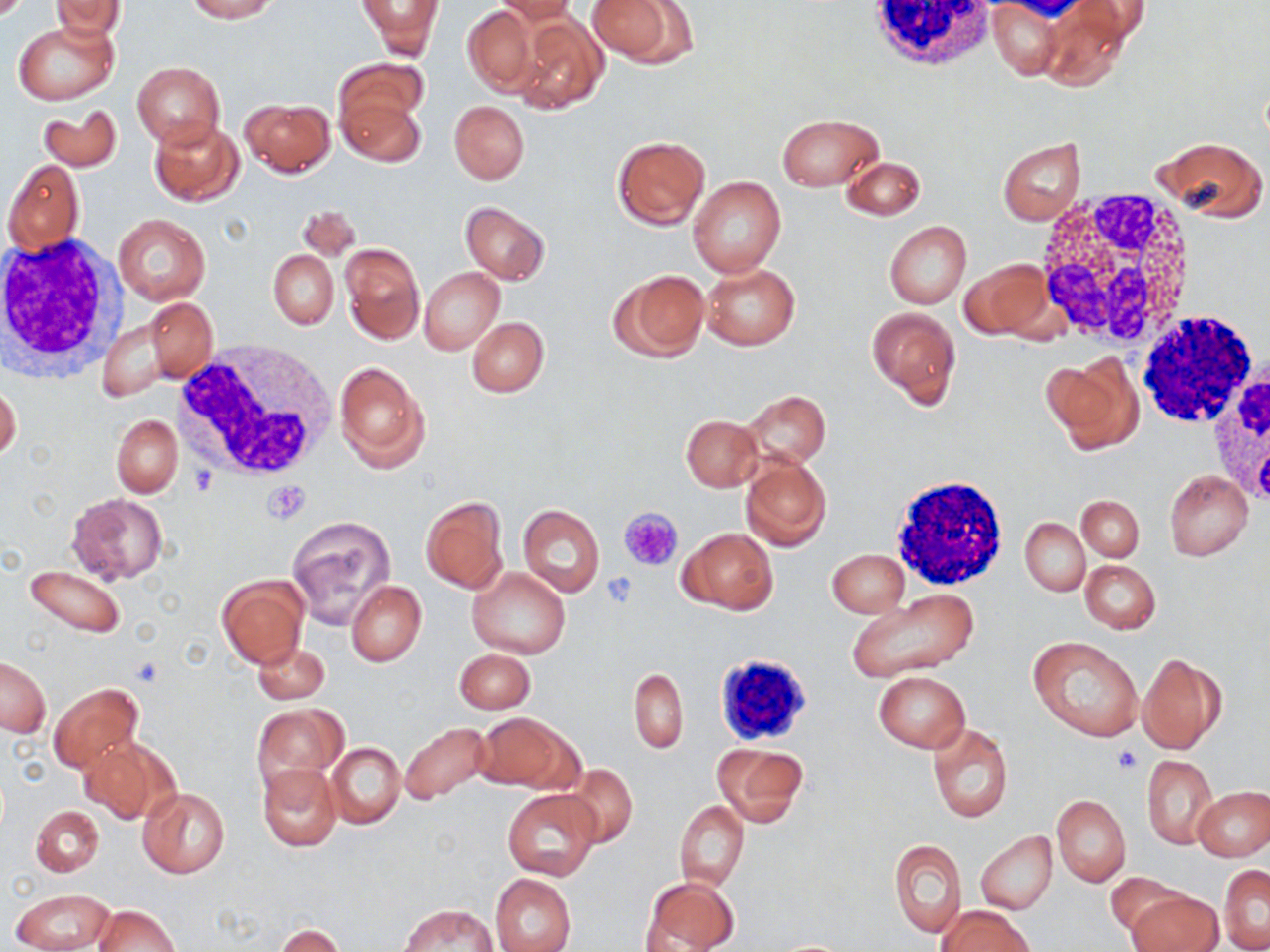

Summary:
  - Coordinate format: approximate bounding boxes as named x1/y1/x2/y2 corners in pixels
  - Platelet locations: (x1=265, y1=481, x2=309, y2=523), (x1=619, y1=506, x2=684, y2=571), (x1=600, y1=571, x2=640, y2=607), (x1=1113, y1=744, x2=1143, y2=773)
  - Uninfected red blood cell locations: (x1=185, y1=0, x2=278, y2=22), (x1=358, y1=0, x2=444, y2=58), (x1=494, y1=0, x2=576, y2=23), (x1=585, y1=0, x2=696, y2=67), (x1=988, y1=0, x2=1065, y2=79), (x1=51, y1=1, x2=126, y2=41), (x1=1039, y1=3, x2=1140, y2=89), (x1=463, y1=5, x2=538, y2=94), (x1=512, y1=11, x2=608, y2=115), (x1=13, y1=20, x2=118, y2=105), (x1=337, y1=57, x2=428, y2=135), (x1=133, y1=62, x2=224, y2=150), (x1=338, y1=96, x2=426, y2=167), (x1=240, y1=97, x2=334, y2=177), (x1=449, y1=100, x2=530, y2=183), (x1=37, y1=106, x2=122, y2=172), (x1=777, y1=113, x2=882, y2=191), (x1=149, y1=118, x2=245, y2=207), (x1=612, y1=136, x2=709, y2=229), (x1=1154, y1=136, x2=1267, y2=223), (x1=998, y1=138, x2=1086, y2=226), (x1=841, y1=155, x2=926, y2=221), (x1=3, y1=159, x2=85, y2=257), (x1=688, y1=175, x2=787, y2=278), (x1=298, y1=202, x2=361, y2=264), (x1=461, y1=202, x2=549, y2=285), (x1=440, y1=209, x2=536, y2=327), (x1=113, y1=212, x2=211, y2=306), (x1=884, y1=220, x2=971, y2=308), (x1=340, y1=242, x2=425, y2=344), (x1=268, y1=250, x2=339, y2=328), (x1=959, y1=258, x2=1057, y2=344), (x1=701, y1=264, x2=800, y2=350), (x1=421, y1=268, x2=504, y2=356), (x1=609, y1=270, x2=710, y2=360), (x1=142, y1=297, x2=219, y2=387), (x1=866, y1=306, x2=961, y2=405), (x1=467, y1=315, x2=548, y2=397), (x1=97, y1=317, x2=174, y2=402), (x1=1043, y1=358, x2=1142, y2=454), (x1=333, y1=359, x2=430, y2=473), (x1=0, y1=384, x2=21, y2=462), (x1=743, y1=390, x2=830, y2=469), (x1=111, y1=414, x2=182, y2=497), (x1=680, y1=414, x2=763, y2=492), (x1=707, y1=429, x2=824, y2=532), (x1=741, y1=454, x2=832, y2=552), (x1=1165, y1=469, x2=1252, y2=560), (x1=66, y1=492, x2=169, y2=585), (x1=1077, y1=495, x2=1144, y2=560), (x1=420, y1=496, x2=508, y2=593), (x1=518, y1=504, x2=605, y2=597), (x1=286, y1=515, x2=396, y2=627), (x1=1021, y1=518, x2=1089, y2=596), (x1=679, y1=528, x2=777, y2=614), (x1=827, y1=549, x2=909, y2=618), (x1=1080, y1=560, x2=1159, y2=633), (x1=23, y1=564, x2=125, y2=637), (x1=467, y1=567, x2=569, y2=658), (x1=216, y1=575, x2=308, y2=668), (x1=346, y1=581, x2=426, y2=666), (x1=845, y1=590, x2=980, y2=683), (x1=1029, y1=636, x2=1143, y2=742), (x1=253, y1=642, x2=330, y2=704), (x1=454, y1=648, x2=535, y2=713), (x1=1137, y1=652, x2=1226, y2=754), (x1=1, y1=656, x2=50, y2=737), (x1=629, y1=668, x2=687, y2=752), (x1=874, y1=671, x2=969, y2=752), (x1=49, y1=682, x2=143, y2=774), (x1=253, y1=703, x2=346, y2=792), (x1=473, y1=711, x2=579, y2=792), (x1=397, y1=722, x2=495, y2=806), (x1=927, y1=723, x2=1013, y2=823), (x1=79, y1=737, x2=177, y2=824), (x1=327, y1=742, x2=405, y2=830), (x1=712, y1=743, x2=809, y2=828), (x1=1142, y1=755, x2=1218, y2=850), (x1=256, y1=763, x2=342, y2=852), (x1=562, y1=765, x2=638, y2=849), (x1=138, y1=787, x2=231, y2=878), (x1=1193, y1=787, x2=1270, y2=860), (x1=502, y1=788, x2=602, y2=882), (x1=1051, y1=796, x2=1130, y2=887), (x1=675, y1=799, x2=749, y2=889), (x1=31, y1=805, x2=103, y2=877), (x1=977, y1=833, x2=1057, y2=914), (x1=890, y1=839, x2=966, y2=937), (x1=1219, y1=864, x2=1270, y2=951), (x1=1105, y1=871, x2=1187, y2=936), (x1=489, y1=873, x2=577, y2=952), (x1=641, y1=875, x2=741, y2=951), (x1=9, y1=887, x2=115, y2=952), (x1=1125, y1=890, x2=1222, y2=952), (x1=92, y1=904, x2=178, y2=952), (x1=398, y1=904, x2=499, y2=951), (x1=938, y1=907, x2=1033, y2=952), (x1=276, y1=925, x2=344, y2=952)
  - White blood cell locations: (x1=862, y1=0, x2=996, y2=71), (x1=1030, y1=192, x2=1199, y2=350), (x1=1, y1=233, x2=125, y2=382), (x1=1133, y1=312, x2=1258, y2=430), (x1=175, y1=342, x2=339, y2=482), (x1=1203, y1=357, x2=1270, y2=504), (x1=887, y1=475, x2=1010, y2=589), (x1=710, y1=652, x2=817, y2=739)
  - Slide-level diagnosis: negative for blood parasites
  - Preparation: thin blood smear
  - Magnification: 1000x
  - Stain: May-Grünwald-Giemsa
  - Image size: 1270×952 pixels
  - Modality: optical microscopy
  - Field of view: single